Give a bounding box for every Plasmodium parasite, every leukocyte, and every artifact (stain precipitate or debris).
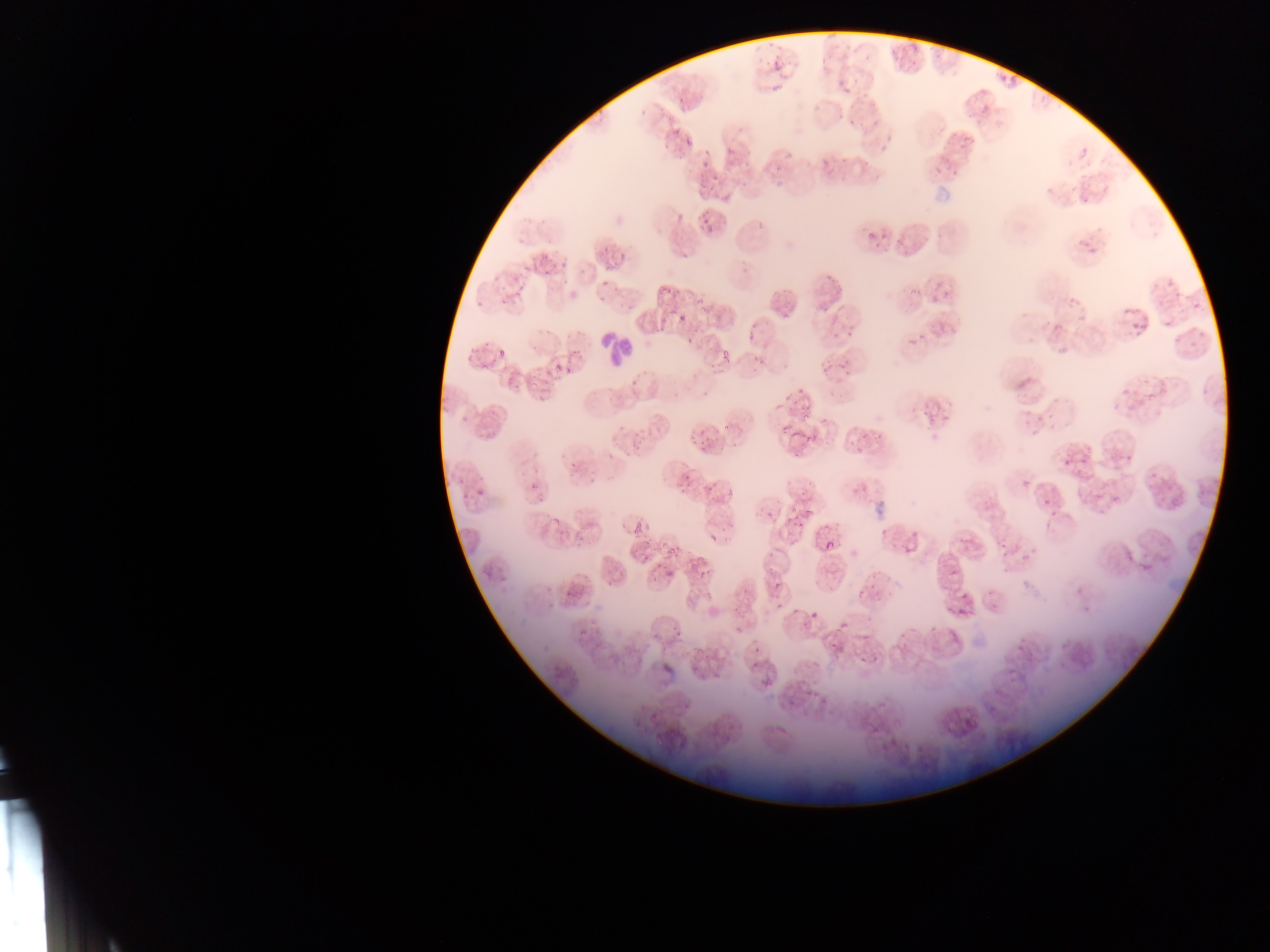

Approximate bounding boxes as [left, top, right, bottom] in pixels.
Plasmodium parasites: [771, 61, 782, 72], [1004, 73, 1018, 88], [841, 83, 853, 100], [846, 117, 856, 125], [669, 124, 677, 135], [680, 132, 695, 146], [956, 132, 976, 151], [877, 143, 891, 154], [726, 146, 734, 157], [820, 158, 829, 166], [699, 162, 709, 169], [771, 163, 784, 171], [935, 166, 943, 178], [949, 167, 958, 178], [708, 174, 721, 185], [701, 183, 713, 191], [1078, 193, 1088, 207], [673, 209, 684, 219], [700, 213, 712, 224], [702, 224, 712, 240], [875, 234, 894, 250], [865, 235, 877, 245], [1076, 237, 1090, 249], [683, 243, 694, 258], [617, 247, 629, 261], [1089, 247, 1097, 255], [530, 251, 545, 272], [559, 262, 567, 269], [605, 262, 617, 274], [539, 266, 555, 278], [825, 269, 837, 281], [491, 273, 505, 284], [602, 275, 613, 286], [835, 277, 848, 297], [652, 279, 677, 301], [1166, 280, 1175, 291], [931, 283, 939, 291], [514, 284, 524, 298], [908, 285, 921, 297], [1174, 285, 1185, 298], [500, 286, 516, 303], [599, 291, 615, 302], [942, 293, 952, 301], [1064, 294, 1081, 311], [929, 297, 940, 308], [698, 299, 709, 310], [820, 299, 830, 321], [1190, 301, 1205, 314], [779, 309, 793, 327], [1075, 312, 1085, 323], [679, 313, 689, 325], [1160, 316, 1177, 330], [1130, 318, 1141, 332], [827, 321, 841, 331], [1141, 322, 1152, 331], [1052, 324, 1063, 332], [747, 326, 757, 341], [932, 326, 943, 334], [840, 330, 857, 343], [831, 332, 838, 342], [685, 334, 695, 346], [1170, 335, 1183, 350], [907, 338, 917, 346], [497, 343, 508, 358], [471, 344, 481, 356], [718, 347, 730, 362], [749, 352, 763, 372], [839, 356, 848, 375], [706, 361, 715, 372], [555, 362, 560, 372], [821, 363, 835, 377], [481, 365, 487, 373], [563, 367, 574, 375], [531, 374, 539, 386], [508, 378, 517, 392], [1123, 381, 1139, 394], [797, 386, 809, 394], [787, 388, 797, 402], [536, 390, 547, 399], [1142, 391, 1156, 404], [800, 406, 812, 421], [1020, 407, 1030, 419], [1034, 412, 1046, 429], [940, 413, 949, 419], [931, 414, 940, 422], [775, 415, 795, 432], [719, 422, 729, 432], [850, 425, 862, 434], [860, 425, 868, 439], [803, 426, 816, 444], [1025, 427, 1042, 441], [689, 428, 697, 440], [697, 430, 705, 436], [872, 434, 881, 445], [632, 436, 647, 449], [849, 440, 860, 448], [700, 445, 710, 455], [855, 448, 864, 456], [790, 451, 799, 463], [1057, 454, 1073, 468], [1117, 454, 1134, 464], [1079, 457, 1090, 465], [569, 462, 576, 472], [1149, 471, 1157, 484], [683, 472, 691, 482], [1016, 477, 1028, 488], [860, 480, 873, 491], [529, 481, 538, 491], [705, 482, 715, 493], [477, 483, 486, 500], [850, 485, 859, 497], [1110, 485, 1122, 499], [676, 487, 684, 495], [1040, 498, 1052, 509], [785, 505, 796, 520], [803, 507, 812, 518], [1049, 509, 1056, 521], [554, 518, 563, 527], [630, 524, 640, 535], [797, 524, 803, 532], [879, 524, 890, 540], [908, 531, 918, 537], [709, 533, 719, 541], [640, 534, 654, 548], [956, 534, 972, 544], [660, 540, 668, 548], [671, 540, 682, 554], [827, 540, 836, 550], [998, 543, 1009, 551], [904, 546, 913, 556], [666, 549, 674, 559], [999, 550, 1010, 562], [1126, 551, 1134, 563], [642, 554, 653, 565], [1019, 554, 1027, 563], [1140, 558, 1152, 572], [657, 563, 665, 570], [617, 567, 625, 577], [668, 567, 678, 578], [949, 568, 957, 581], [700, 571, 707, 579], [868, 572, 884, 583], [651, 575, 659, 584], [771, 582, 782, 594], [1076, 585, 1086, 599], [739, 588, 748, 596], [858, 588, 865, 600], [958, 589, 969, 603], [704, 590, 713, 600], [873, 590, 881, 604], [991, 597, 998, 611], [774, 603, 782, 611], [791, 604, 802, 615], [734, 605, 746, 618], [944, 605, 950, 614], [956, 608, 968, 618], [809, 611, 817, 621], [837, 620, 847, 633], [799, 622, 809, 628], [929, 622, 938, 635], [671, 623, 685, 636], [735, 625, 745, 635], [908, 626, 916, 637], [895, 629, 908, 642], [579, 630, 586, 638], [862, 631, 870, 643], [1015, 637, 1028, 651], [830, 640, 839, 654], [659, 643, 669, 655], [753, 646, 762, 653], [860, 656, 868, 663], [872, 658, 882, 664], [813, 659, 825, 670], [750, 661, 758, 670], [689, 662, 696, 675], [706, 666, 725, 681], [1008, 677, 1016, 687], [762, 679, 771, 690], [805, 690, 815, 699], [817, 692, 828, 710], [683, 699, 693, 714], [648, 709, 661, 723] | approximate [x, y] pixel centers of objects too small to bound: [924, 413], [1085, 609], [1010, 671].
Leukocytes: [588, 318, 640, 373].

Thin blood film. Image is 1270×952 pixels. Photographed through a microscope with a mobile-phone camera. One field of view. Sample from Ghana.